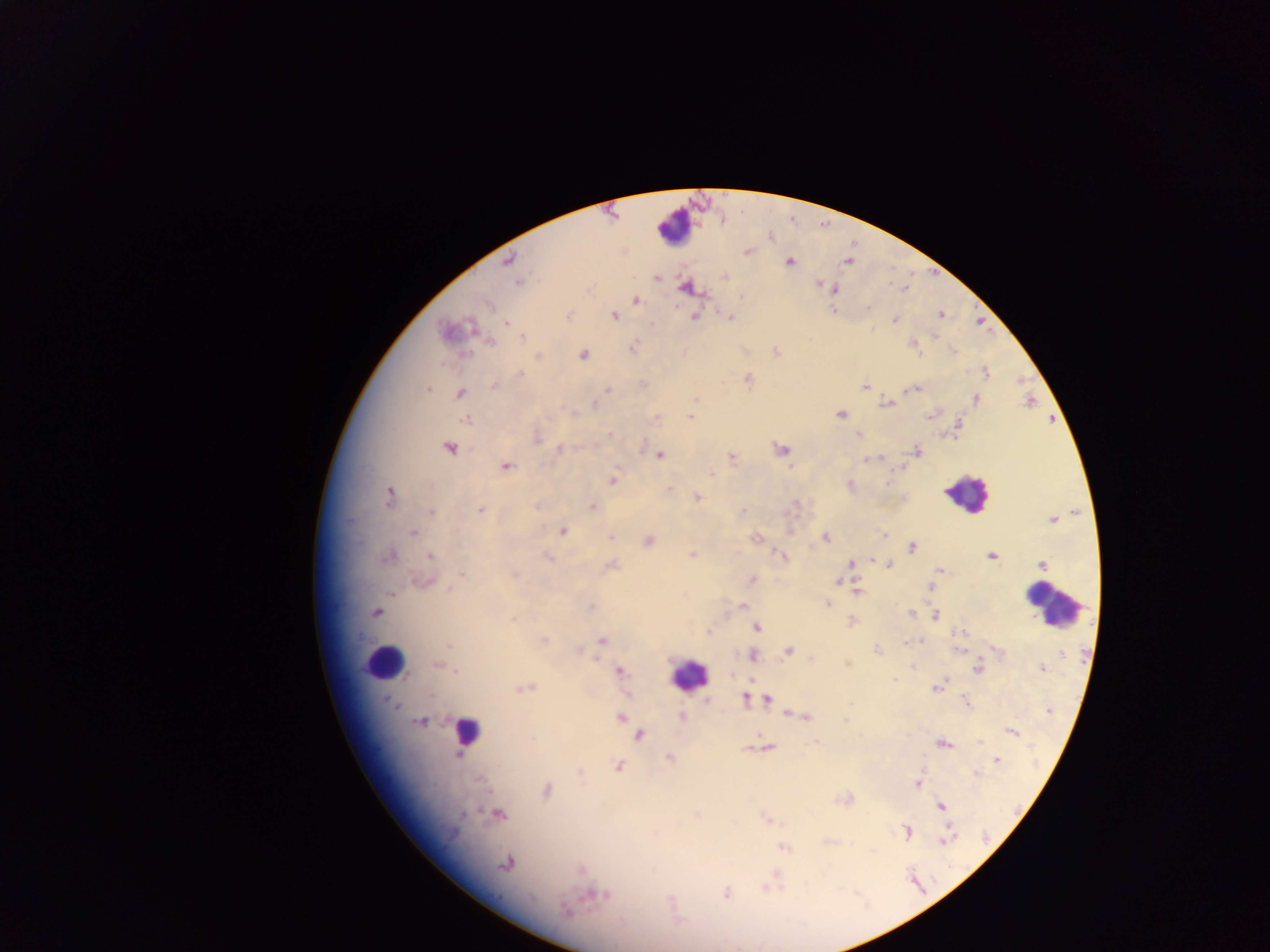

Approximate centers as {x, y} in pixels.
Summary:
  - Leukocyte locations: {675, 228}, {965, 493}, {1052, 604}, {384, 662}, {688, 676}, {465, 730}
  - Plasmodium parasite locations: {747, 251}, {507, 261}, {789, 261}, {847, 261}, {724, 275}, {656, 278}, {519, 283}, {818, 283}, {687, 287}, {903, 288}, {834, 289}, {635, 300}, {489, 303}, {833, 310}, {940, 314}, {567, 315}, {614, 315}, {695, 316}, {728, 316}, {894, 320}, {506, 322}, {446, 331}, {521, 337}, {490, 342}, {912, 344}, {631, 348}, {775, 351}, {952, 351}, {684, 353}, {583, 354}, {538, 356}, {986, 372}, {520, 374}, {747, 378}, {494, 386}, {865, 386}, {428, 389}, {914, 389}, {607, 390}, {460, 393}, {975, 399}, {1029, 401}, {887, 403}, {594, 405}, {572, 413}, {932, 413}, {691, 415}, {840, 415}, {467, 419}, {957, 428}, {858, 434}, {609, 435}, {536, 436}, {449, 447}, {559, 448}, {780, 449}, {916, 451}, {659, 455}, {731, 457}, {867, 459}, {505, 466}, {710, 472}, {612, 479}, {850, 485}, {667, 489}, {388, 496}, {696, 498}, {537, 505}, {592, 506}, {481, 509}, {430, 512}, {741, 512}, {1052, 520}, {788, 529}, {562, 530}, {413, 533}, {883, 535}, {609, 536}, {825, 537}, {755, 538}, {648, 541}, {911, 547}, {692, 554}, {388, 556}, {430, 556}, {781, 556}, {991, 556}, {549, 557}, {888, 563}, {851, 564}, {1042, 564}, {611, 565}, {940, 569}, {462, 573}, {514, 574}, {937, 575}, {752, 580}, {423, 581}, {836, 582}, {931, 587}, {856, 590}, {827, 605}, {590, 607}, {742, 607}, {375, 612}, {910, 613}, {936, 615}, {513, 619}, {852, 622}, {756, 627}, {708, 631}, {542, 640}, {601, 640}, {920, 640}, {906, 643}, {449, 646}, {578, 649}, {959, 649}, {877, 650}, {787, 651}, {1000, 652}, {1060, 653}, {752, 655}, {810, 658}, {846, 662}, {437, 664}, {913, 667}, {977, 667}, {456, 669}, {1042, 669}, {618, 671}, {893, 678}, {752, 681}, {936, 686}, {523, 688}, {626, 694}, {745, 698}, {758, 698}, {767, 699}, {707, 701}, {966, 702}, {788, 713}, {681, 716}, {806, 716}, {620, 717}, {846, 720}, {421, 722}, {1011, 731}, {639, 734}, {979, 741}, {942, 743}, {766, 747}, {457, 755}, {669, 758}, {997, 759}, {618, 766}, {579, 772}, {975, 773}, {917, 783}, {546, 790}, {941, 805}, {497, 814}, {694, 814}, {767, 819}, {907, 831}, {654, 834}, {945, 840}, {782, 847}, {506, 863}, {580, 868}, {726, 893}, {595, 894}, {565, 911}
  - Image size: 1270×952 pixels
  - Capture: mobile-phone photograph through a microscope
  - Country: Ghana
  - Preparation: thick blood smear
  - Field of view: single